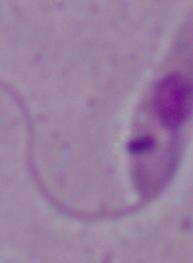
magnification = 1000x
identification = Leishmania
modality = photomicrograph